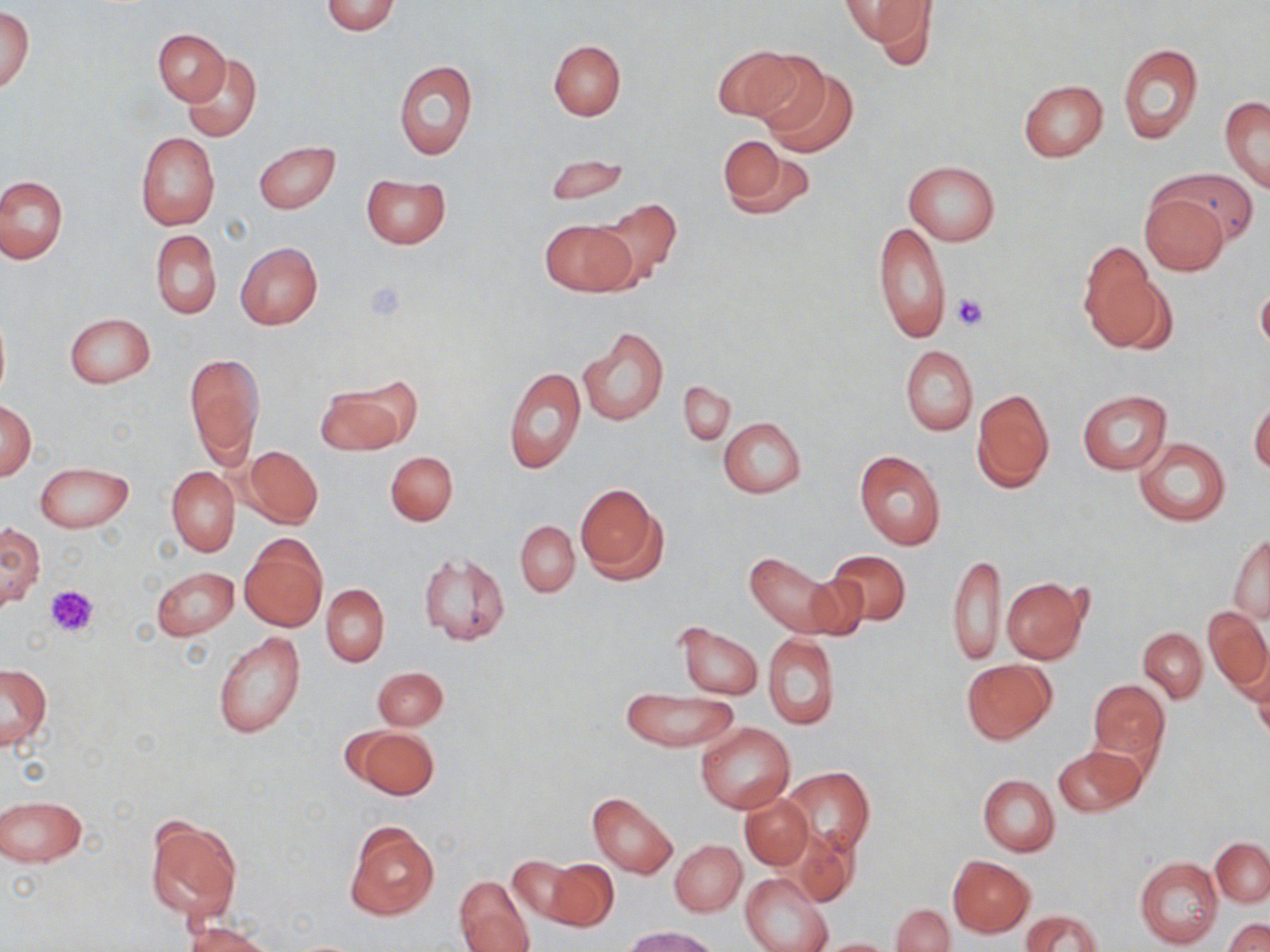

Summary:
  - Coordinate format: approximate bounding boxes as named x1/y1/x2/y2 corners in pixels
  - Uninfected red blood cell locations: (x1=837, y1=0, x2=935, y2=53), (x1=321, y1=1, x2=402, y2=35), (x1=0, y1=6, x2=35, y2=94), (x1=154, y1=29, x2=230, y2=105), (x1=548, y1=39, x2=626, y2=120), (x1=1117, y1=43, x2=1203, y2=143), (x1=716, y1=45, x2=821, y2=128), (x1=183, y1=54, x2=262, y2=142), (x1=393, y1=59, x2=479, y2=160), (x1=758, y1=62, x2=858, y2=157), (x1=1018, y1=80, x2=1109, y2=162), (x1=1219, y1=97, x2=1270, y2=193), (x1=135, y1=132, x2=220, y2=230), (x1=716, y1=138, x2=812, y2=219), (x1=254, y1=142, x2=340, y2=214), (x1=542, y1=153, x2=628, y2=205), (x1=903, y1=160, x2=999, y2=245), (x1=1165, y1=168, x2=1257, y2=245), (x1=361, y1=174, x2=451, y2=249), (x1=0, y1=177, x2=67, y2=263), (x1=1140, y1=191, x2=1229, y2=275), (x1=596, y1=198, x2=681, y2=289), (x1=540, y1=218, x2=634, y2=296), (x1=873, y1=220, x2=950, y2=343), (x1=151, y1=230, x2=222, y2=319), (x1=235, y1=242, x2=323, y2=330), (x1=1079, y1=245, x2=1169, y2=351), (x1=1257, y1=285, x2=1270, y2=355), (x1=0, y1=311, x2=10, y2=405), (x1=64, y1=312, x2=156, y2=388), (x1=578, y1=327, x2=669, y2=426), (x1=900, y1=345, x2=978, y2=435), (x1=185, y1=352, x2=263, y2=467), (x1=503, y1=366, x2=585, y2=475), (x1=680, y1=380, x2=734, y2=444), (x1=317, y1=384, x2=406, y2=454), (x1=972, y1=389, x2=1054, y2=492), (x1=1077, y1=390, x2=1171, y2=474), (x1=1, y1=400, x2=36, y2=480), (x1=1249, y1=400, x2=1270, y2=475), (x1=719, y1=417, x2=806, y2=497), (x1=1133, y1=437, x2=1231, y2=526), (x1=243, y1=446, x2=323, y2=528), (x1=854, y1=450, x2=947, y2=550), (x1=385, y1=451, x2=458, y2=525), (x1=36, y1=460, x2=133, y2=533), (x1=167, y1=466, x2=239, y2=556), (x1=574, y1=484, x2=666, y2=584), (x1=515, y1=521, x2=579, y2=596), (x1=0, y1=522, x2=42, y2=611), (x1=239, y1=534, x2=328, y2=632), (x1=1228, y1=535, x2=1269, y2=622), (x1=823, y1=549, x2=912, y2=628), (x1=743, y1=551, x2=854, y2=639), (x1=418, y1=552, x2=510, y2=645), (x1=947, y1=553, x2=1006, y2=667), (x1=151, y1=566, x2=238, y2=640), (x1=1002, y1=578, x2=1087, y2=664), (x1=321, y1=584, x2=389, y2=666), (x1=1205, y1=605, x2=1270, y2=695), (x1=674, y1=623, x2=763, y2=699), (x1=1138, y1=628, x2=1207, y2=703), (x1=212, y1=633, x2=306, y2=738), (x1=764, y1=634, x2=840, y2=729), (x1=1244, y1=653, x2=1270, y2=738), (x1=961, y1=659, x2=1056, y2=743), (x1=1, y1=664, x2=52, y2=750), (x1=372, y1=667, x2=448, y2=729), (x1=1087, y1=678, x2=1170, y2=774), (x1=621, y1=689, x2=738, y2=751), (x1=696, y1=723, x2=795, y2=813), (x1=350, y1=725, x2=439, y2=799), (x1=1053, y1=745, x2=1147, y2=817), (x1=785, y1=767, x2=873, y2=856), (x1=979, y1=775, x2=1060, y2=855), (x1=587, y1=792, x2=677, y2=878), (x1=1, y1=795, x2=86, y2=866), (x1=741, y1=795, x2=812, y2=869), (x1=143, y1=814, x2=242, y2=925), (x1=344, y1=820, x2=439, y2=920), (x1=785, y1=826, x2=860, y2=907), (x1=1211, y1=838, x2=1269, y2=907), (x1=670, y1=840, x2=746, y2=915), (x1=947, y1=854, x2=1034, y2=936), (x1=1134, y1=855, x2=1223, y2=948), (x1=509, y1=856, x2=583, y2=926), (x1=543, y1=857, x2=619, y2=931), (x1=741, y1=872, x2=833, y2=952), (x1=455, y1=874, x2=535, y2=950), (x1=891, y1=903, x2=955, y2=952), (x1=1022, y1=910, x2=1102, y2=952), (x1=1224, y1=918, x2=1270, y2=952), (x1=185, y1=921, x2=273, y2=952), (x1=625, y1=926, x2=723, y2=952), (x1=811, y1=938, x2=899, y2=951)
  - Platelet locations: (x1=364, y1=281, x2=407, y2=322), (x1=952, y1=294, x2=988, y2=331), (x1=46, y1=583, x2=101, y2=638)
  - Slide-level diagnosis: no evidence of blood parasites
  - Modality: optical microscopy
  - Field of view: single
  - Image size: 1270×952 pixels
  - Stain: May-Grünwald-Giemsa
  - Magnification: 1000x
  - Preparation: thin blood film